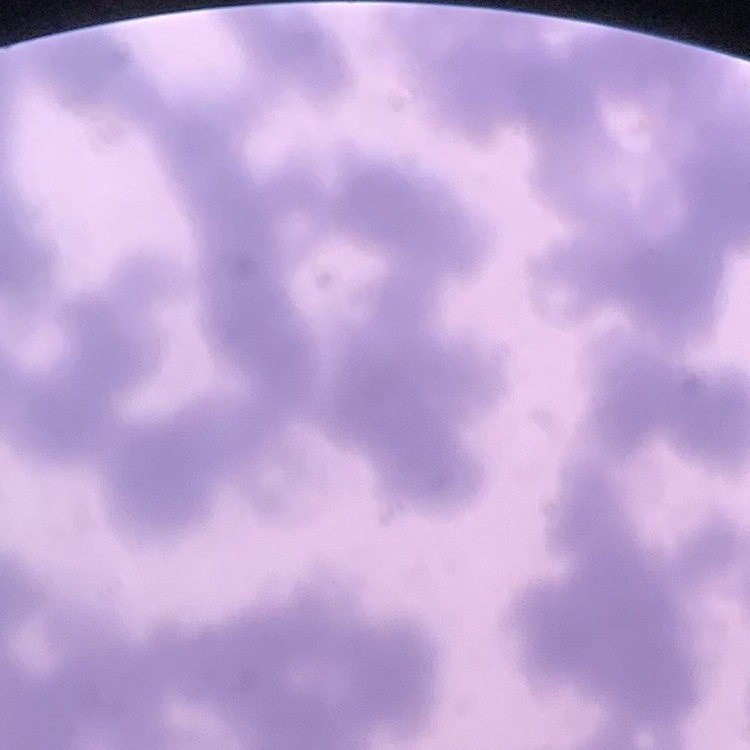

The erythrocytes exhibit rouleaux formation. Thin blood smear. One tile cut from a larger photomicrograph. Stained with either Field's or Giemsa.